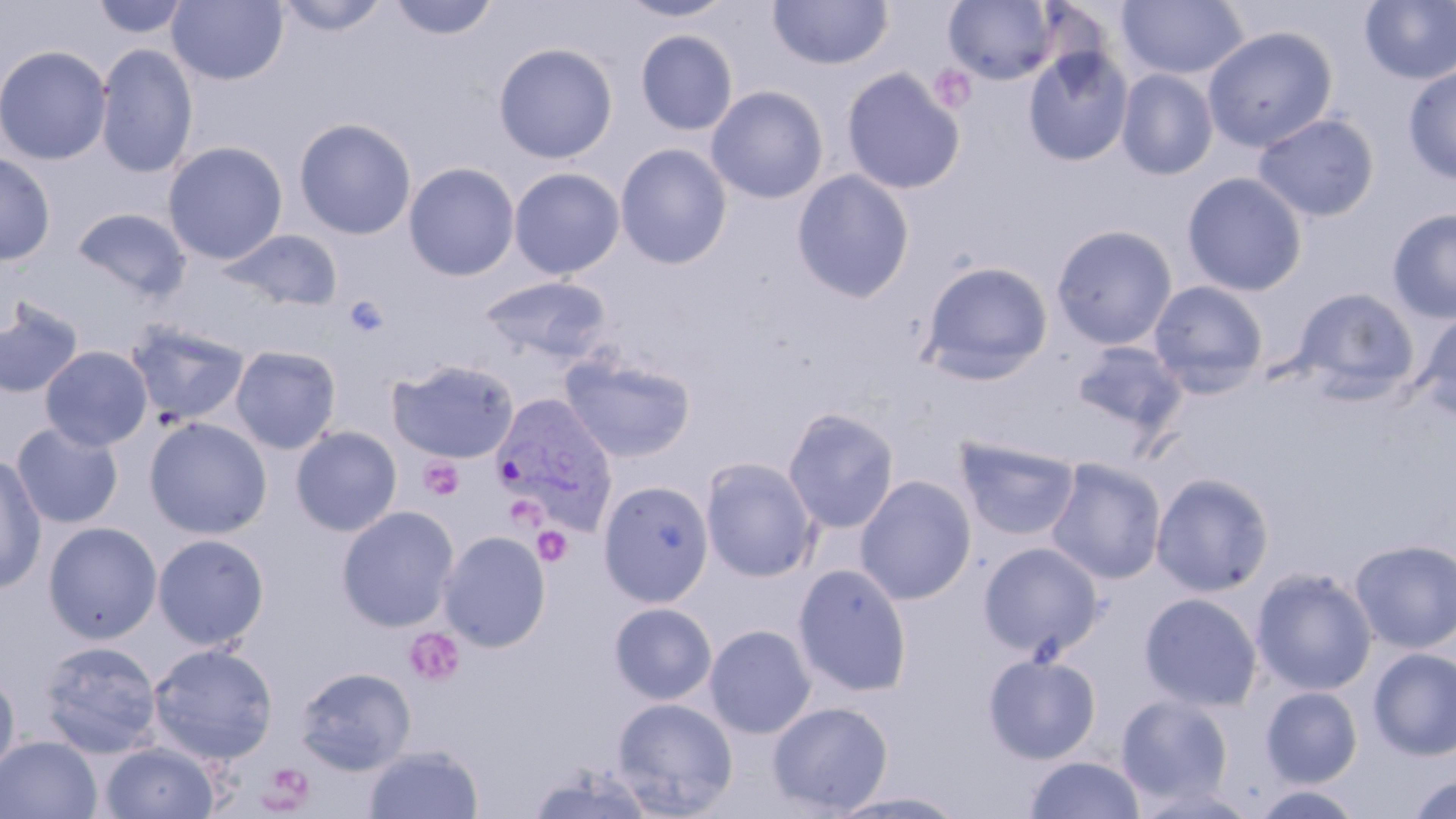

{
  "slide_level_diagnosis": "Plasmodium vivax",
  "image_size": "1456×819 pixels",
  "modality": "light microscopy",
  "field_of_view": "one of a larger specimen",
  "preparation": "thin blood film",
  "platelet_locations": "approximate bounding boxes as (x1,y1)-(x2,y2) corner pairs in pixels: (929,64)-(978,113), (343,295)-(389,337), (419,457)-(463,500), (504,498)-(548,534), (532,526)-(573,567), (405,627)-(466,687), (258,762)-(316,812)",
  "plasmodium_vivax_infected_red_blood_cell_locations": "approximate bounding boxes as (x1,y1)-(x2,y2) corner pairs in pixels: (492,393)-(618,525)",
  "magnification": "1000x",
  "stain": "May-Grünwald-Giemsa",
  "uninfected_red_blood_cell_locations": "approximate bounding boxes as (x1,y1)-(x2,y2) corner pairs in pixels: (91,0)-(192,39), (275,0)-(391,35), (389,0)-(499,41), (617,0)-(736,22), (767,0)-(893,71), (1116,0)-(1249,80), (167,1)-(289,85), (944,1)-(1058,85), (1359,1)-(1456,84), (1202,26)-(1338,152), (635,29)-(738,135), (493,42)-(618,163), (0,44)-(112,165), (95,44)-(198,179), (1023,47)-(1133,166), (1403,65)-(1456,185), (842,68)-(965,194), (1116,69)-(1218,180), (705,85)-(829,204), (1253,112)-(1379,221), (294,117)-(417,240), (163,141)-(288,265), (615,143)-(733,270), (0,151)-(56,265), (403,162)-(520,281), (509,167)-(625,279), (791,170)-(915,303), (1182,171)-(1308,297), (72,207)-(191,301), (1387,207)-(1456,323), (1051,224)-(1178,350), (220,228)-(343,311), (917,260)-(1054,385), (478,274)-(613,365), (1147,280)-(1269,395), (1291,287)-(1421,402), (0,299)-(84,399), (1414,312)-(1456,421), (125,322)-(251,426), (1070,340)-(1189,441), (230,345)-(342,454), (40,346)-(153,451), (560,352)-(696,463), (387,359)-(519,463), (782,406)-(900,534), (144,417)-(272,539), (11,422)-(123,528), (290,426)-(402,536), (953,435)-(1081,542), (0,453)-(46,593), (700,457)-(820,582), (1045,457)-(1167,585), (1151,472)-(1275,596), (854,475)-(977,605), (598,479)-(715,607), (337,505)-(460,632), (43,521)-(163,644), (438,530)-(551,652), (152,534)-(269,650), (1349,537)-(1456,653), (979,542)-(1103,658), (792,562)-(913,697), (1251,568)-(1377,695), (1140,592)-(1262,711), (608,602)-(717,704), (704,624)-(816,738), (39,640)-(162,758), (148,642)-(279,764), (1368,647)-(1456,760), (982,653)-(1101,764), (294,666)-(416,775), (0,669)-(19,784), (1260,685)-(1363,787), (1116,693)-(1234,804), (611,696)-(738,818), (767,701)-(893,815), (0,735)-(102,818), (100,741)-(220,819), (363,744)-(483,819), (1024,756)-(1146,818), (523,762)-(657,818), (1406,774)-(1456,818), (1249,785)-(1367,819), (827,789)-(971,817)"
}